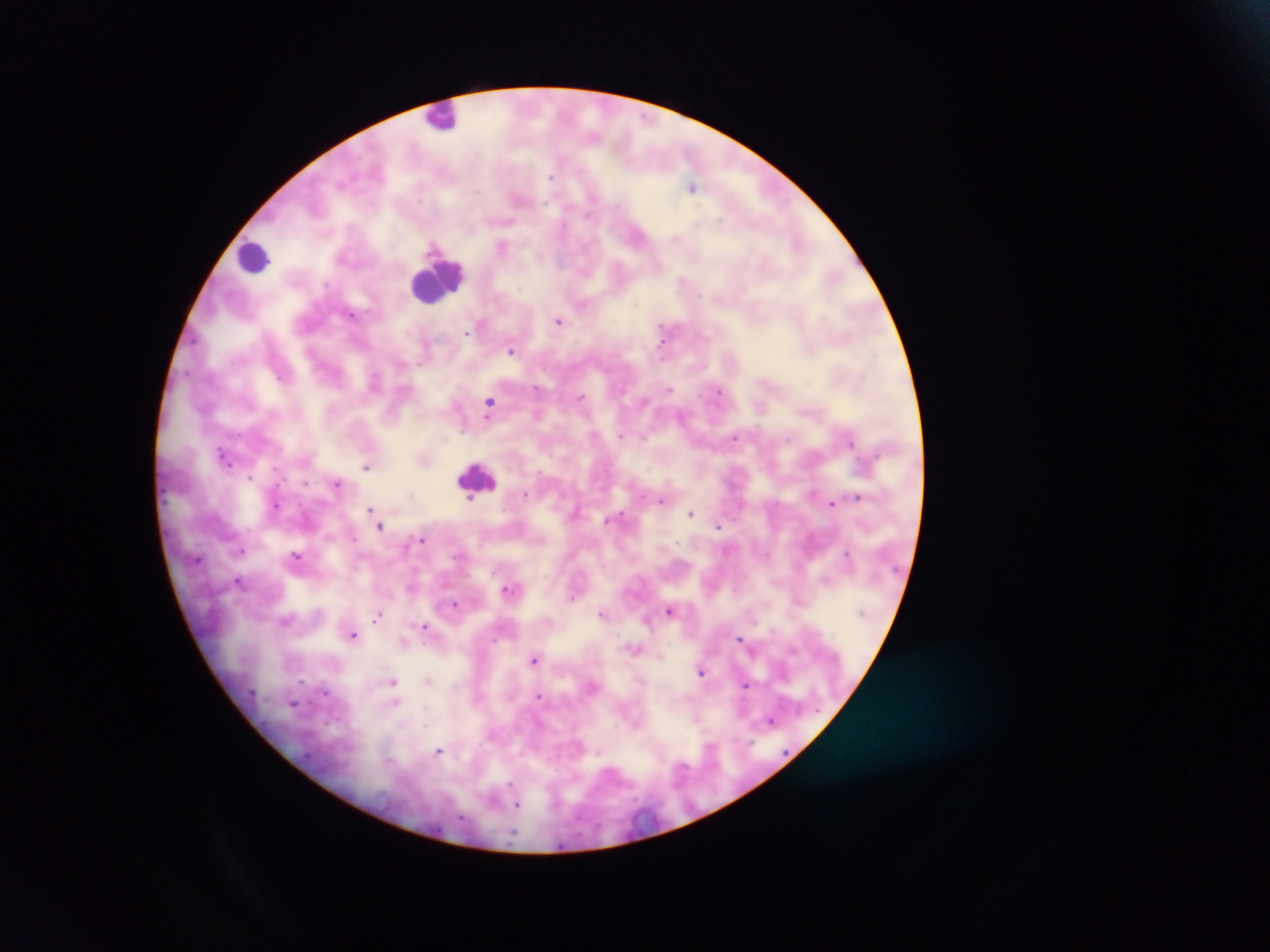

Approximate centers as [x, y] in pixels.
Summary:
  - Leukocyte locations: [444, 116], [254, 257], [434, 281], [479, 472]
  - Malaria parasite locations: [595, 137], [551, 177], [692, 186], [506, 221], [674, 238], [501, 246], [658, 266], [682, 280], [326, 285], [351, 314], [558, 321], [662, 326], [466, 332], [662, 343], [510, 351], [281, 377], [375, 379], [537, 388], [668, 390], [719, 391], [580, 397], [490, 402], [682, 416], [463, 429], [595, 434], [620, 436], [643, 437], [735, 437], [789, 440], [850, 443], [225, 456], [366, 466], [250, 477], [337, 483], [525, 494], [858, 497], [471, 498], [660, 502], [832, 503], [276, 505], [371, 509], [690, 513], [717, 526], [380, 527], [354, 538], [422, 540], [240, 550], [847, 553], [296, 556], [825, 579], [238, 581], [508, 589], [572, 597], [454, 603], [669, 610], [602, 613], [378, 616], [424, 626], [353, 635], [740, 638], [793, 649], [534, 660], [701, 672], [428, 680], [301, 681], [393, 681], [745, 686], [325, 692], [538, 696], [395, 703], [294, 704], [697, 717], [771, 720], [710, 747], [439, 751], [599, 752], [681, 768], [510, 787], [493, 799], [517, 805]
  - Image size: 1270×952 pixels
  - Country: Ghana
  - Field of view: single
  - Capture: mobile-phone photograph through a microscope
  - Preparation: thick blood smear